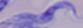

A trypanosome is seen. 1000x magnification. Photomicrograph.